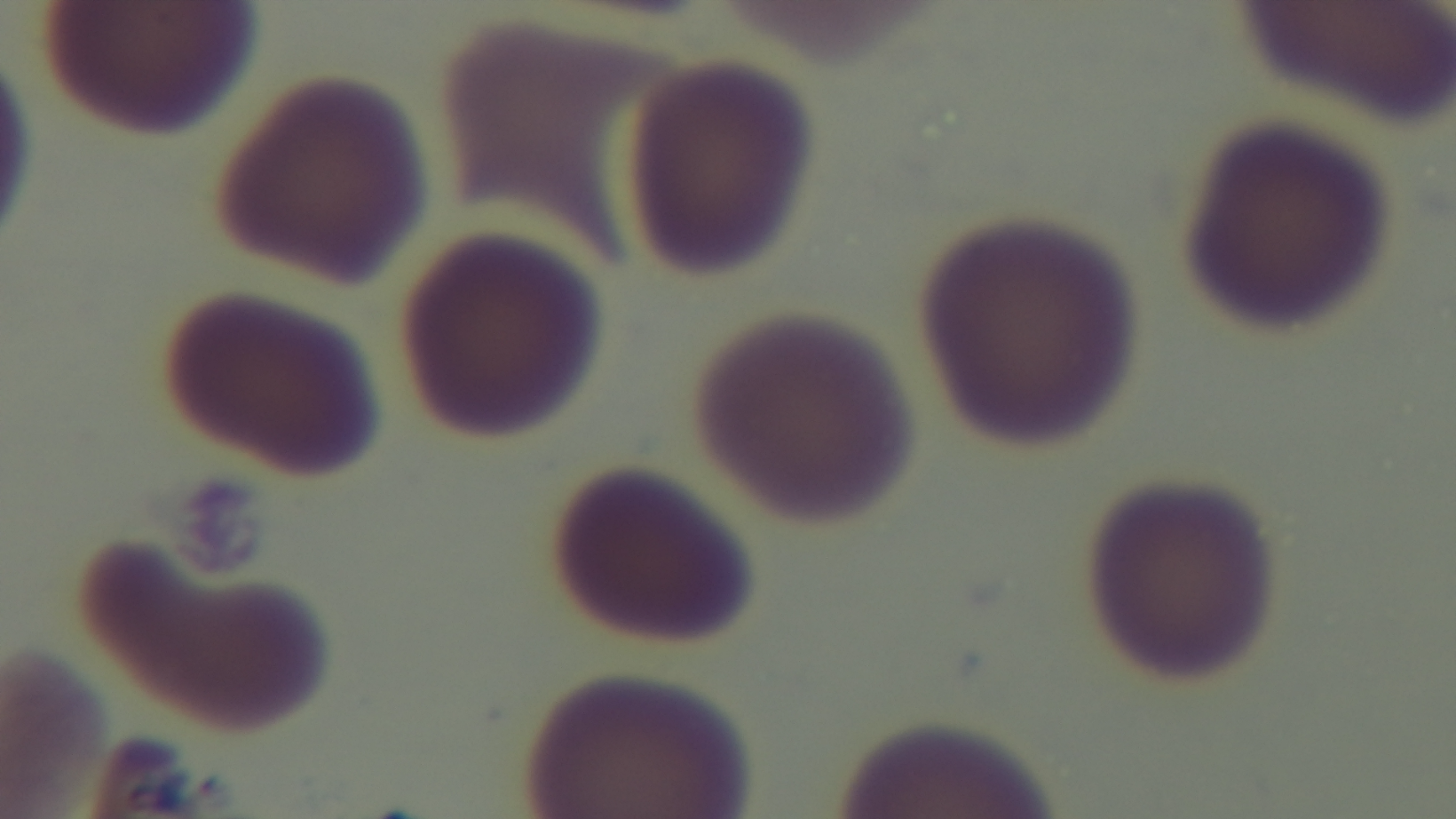

Summary:
  - Stain: Giemsa
  - Malaria status: uninfected
  - Capture: mounted 4K digital camera
  - Modality: light microscopy
  - Field of view: one from the slide
  - Preparation: thin
  - Objective: 100x oil immersion